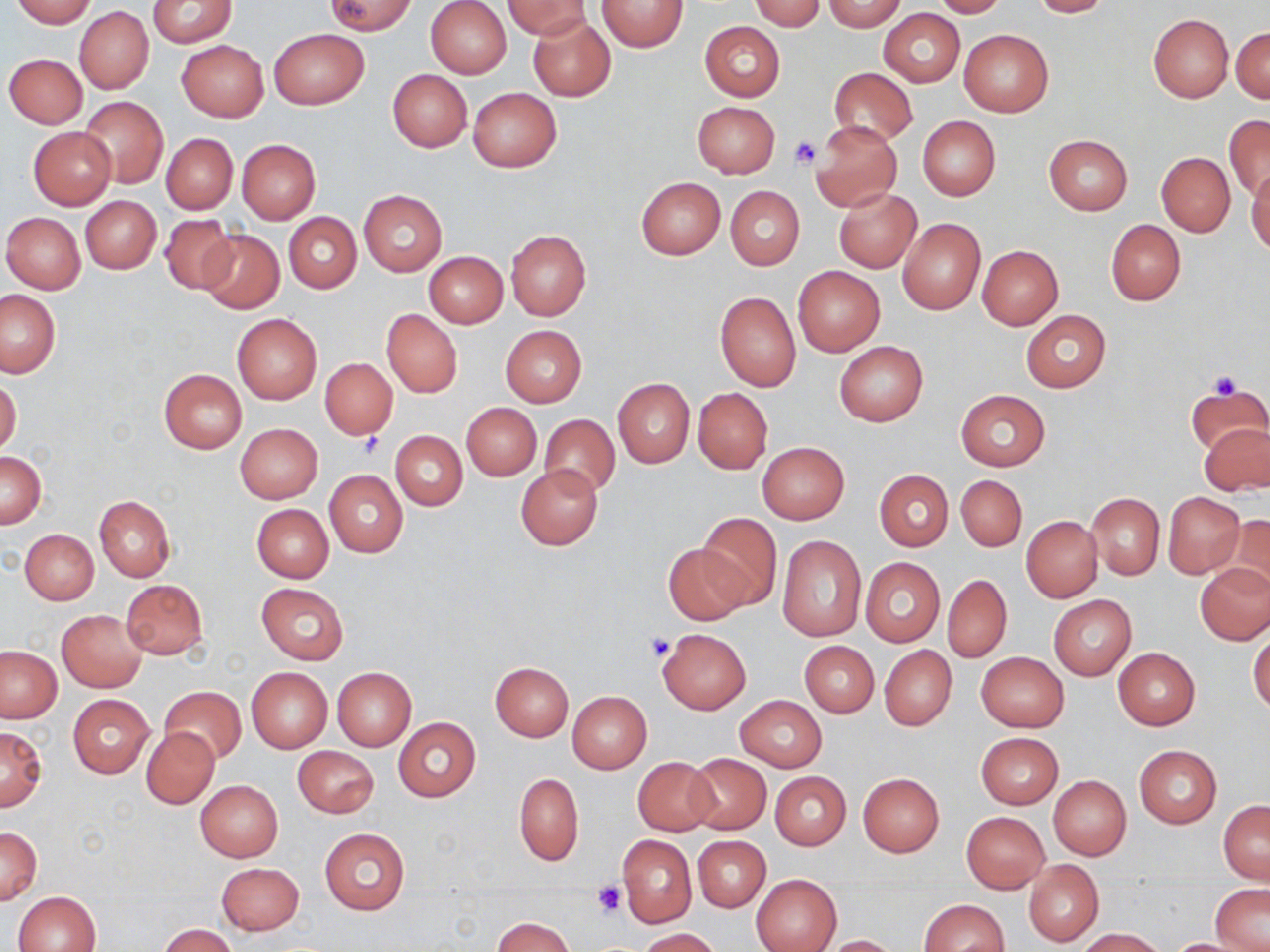 Approximate bounding boxes as named x1/y1/x2/y2 corners in pixels. Platelet locations: (x1=790, y1=136, x2=822, y2=170), (x1=1206, y1=370, x2=1246, y2=402), (x1=352, y1=433, x2=386, y2=460), (x1=645, y1=633, x2=674, y2=662), (x1=591, y1=881, x2=625, y2=917). Uninfected red blood cell locations: (x1=10, y1=0, x2=96, y2=26), (x1=148, y1=0, x2=237, y2=47), (x1=326, y1=0, x2=415, y2=34), (x1=425, y1=0, x2=512, y2=78), (x1=749, y1=0, x2=826, y2=30), (x1=932, y1=0, x2=1007, y2=18), (x1=1028, y1=0, x2=1113, y2=17), (x1=505, y1=1, x2=590, y2=39), (x1=598, y1=1, x2=688, y2=52), (x1=821, y1=1, x2=908, y2=31), (x1=74, y1=6, x2=154, y2=95), (x1=879, y1=8, x2=964, y2=87), (x1=1148, y1=14, x2=1234, y2=103), (x1=527, y1=15, x2=615, y2=102), (x1=699, y1=21, x2=785, y2=100), (x1=1231, y1=26, x2=1270, y2=103), (x1=269, y1=28, x2=368, y2=109), (x1=959, y1=28, x2=1054, y2=118), (x1=177, y1=39, x2=268, y2=121), (x1=4, y1=53, x2=87, y2=128), (x1=829, y1=68, x2=917, y2=146), (x1=387, y1=69, x2=472, y2=152), (x1=467, y1=87, x2=561, y2=172), (x1=80, y1=97, x2=168, y2=189), (x1=692, y1=101, x2=780, y2=178), (x1=1224, y1=115, x2=1270, y2=202), (x1=917, y1=116, x2=1000, y2=200), (x1=810, y1=121, x2=901, y2=213), (x1=27, y1=126, x2=117, y2=208), (x1=162, y1=133, x2=237, y2=214), (x1=1044, y1=135, x2=1133, y2=216), (x1=236, y1=139, x2=320, y2=223), (x1=1156, y1=152, x2=1235, y2=236), (x1=1246, y1=168, x2=1270, y2=256), (x1=635, y1=177, x2=725, y2=259), (x1=833, y1=185, x2=921, y2=272), (x1=726, y1=186, x2=804, y2=270), (x1=358, y1=189, x2=446, y2=276), (x1=82, y1=196, x2=162, y2=274), (x1=2, y1=212, x2=85, y2=293), (x1=284, y1=212, x2=361, y2=293), (x1=158, y1=214, x2=237, y2=294), (x1=897, y1=218, x2=985, y2=314), (x1=1105, y1=219, x2=1186, y2=306), (x1=197, y1=230, x2=282, y2=314), (x1=506, y1=230, x2=591, y2=320), (x1=977, y1=245, x2=1063, y2=329), (x1=423, y1=251, x2=507, y2=327), (x1=793, y1=267, x2=884, y2=356), (x1=0, y1=290, x2=60, y2=377), (x1=715, y1=290, x2=801, y2=392), (x1=382, y1=309, x2=462, y2=397), (x1=1020, y1=310, x2=1111, y2=392), (x1=231, y1=312, x2=322, y2=405), (x1=500, y1=325, x2=586, y2=407), (x1=834, y1=341, x2=928, y2=425), (x1=319, y1=357, x2=397, y2=440), (x1=159, y1=369, x2=247, y2=452), (x1=0, y1=377, x2=21, y2=456), (x1=612, y1=378, x2=695, y2=468), (x1=1184, y1=384, x2=1269, y2=459), (x1=693, y1=388, x2=771, y2=474), (x1=955, y1=389, x2=1049, y2=471), (x1=461, y1=403, x2=542, y2=480), (x1=539, y1=414, x2=620, y2=499), (x1=1200, y1=421, x2=1269, y2=495), (x1=235, y1=423, x2=323, y2=503), (x1=390, y1=431, x2=468, y2=510), (x1=757, y1=441, x2=850, y2=523), (x1=1, y1=450, x2=46, y2=529), (x1=516, y1=465, x2=603, y2=549), (x1=324, y1=470, x2=408, y2=557), (x1=875, y1=470, x2=953, y2=550), (x1=955, y1=474, x2=1027, y2=551), (x1=1162, y1=492, x2=1245, y2=578), (x1=1085, y1=493, x2=1164, y2=579), (x1=94, y1=496, x2=175, y2=581), (x1=251, y1=503, x2=333, y2=582), (x1=697, y1=512, x2=782, y2=612), (x1=1222, y1=515, x2=1270, y2=600), (x1=1021, y1=516, x2=1102, y2=602), (x1=20, y1=529, x2=99, y2=604), (x1=778, y1=536, x2=866, y2=641), (x1=662, y1=541, x2=750, y2=626), (x1=860, y1=558, x2=945, y2=646), (x1=1196, y1=563, x2=1270, y2=644), (x1=942, y1=574, x2=1012, y2=664), (x1=121, y1=579, x2=207, y2=660), (x1=256, y1=583, x2=349, y2=665), (x1=1049, y1=595, x2=1136, y2=679), (x1=57, y1=610, x2=147, y2=692), (x1=1248, y1=627, x2=1270, y2=715), (x1=657, y1=628, x2=751, y2=713), (x1=799, y1=640, x2=879, y2=718), (x1=880, y1=645, x2=956, y2=730), (x1=0, y1=646, x2=62, y2=723), (x1=1113, y1=647, x2=1199, y2=729), (x1=976, y1=651, x2=1068, y2=732), (x1=490, y1=661, x2=573, y2=740), (x1=247, y1=666, x2=332, y2=753), (x1=332, y1=667, x2=416, y2=750), (x1=159, y1=687, x2=246, y2=765), (x1=567, y1=691, x2=651, y2=773), (x1=67, y1=693, x2=155, y2=777), (x1=735, y1=695, x2=825, y2=772), (x1=393, y1=717, x2=481, y2=802), (x1=0, y1=725, x2=46, y2=811), (x1=141, y1=727, x2=219, y2=808), (x1=975, y1=731, x2=1063, y2=808), (x1=292, y1=745, x2=379, y2=818), (x1=1133, y1=745, x2=1221, y2=828), (x1=684, y1=753, x2=770, y2=834), (x1=632, y1=756, x2=718, y2=835), (x1=770, y1=771, x2=851, y2=850), (x1=513, y1=772, x2=583, y2=866), (x1=858, y1=772, x2=945, y2=856), (x1=1048, y1=775, x2=1131, y2=860), (x1=196, y1=780, x2=283, y2=862), (x1=1219, y1=801, x2=1269, y2=883), (x1=961, y1=811, x2=1049, y2=893), (x1=320, y1=827, x2=409, y2=915), (x1=1, y1=828, x2=41, y2=905), (x1=618, y1=835, x2=696, y2=927), (x1=693, y1=836, x2=770, y2=912), (x1=1023, y1=860, x2=1104, y2=946), (x1=215, y1=862, x2=304, y2=936), (x1=752, y1=874, x2=842, y2=952), (x1=1212, y1=886, x2=1270, y2=951), (x1=14, y1=891, x2=101, y2=952), (x1=918, y1=899, x2=1009, y2=952), (x1=493, y1=917, x2=576, y2=952), (x1=158, y1=924, x2=236, y2=952), (x1=638, y1=928, x2=721, y2=951), (x1=1076, y1=928, x2=1167, y2=951), (x1=822, y1=934, x2=904, y2=952), (x1=1162, y1=938, x2=1259, y2=951). Slide-level diagnosis: no evidence of blood parasites. May-Grünwald-Giemsa-stained preparation. Captured at 1000x magnification. Image is 1270×952 pixels. Single field of view. Optical microscopy. Thin blood film.